Assess this cell for malaria.
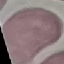

Uninfected.

Giemsa-stained preparation. Photographed with a smartphone camera at the microscope eyepiece. Thin blood film. Cell patch, automatically extracted from a larger field of view and resized to 64 × 64 pixels.